Assess this cell for malaria.
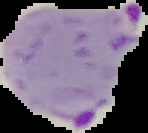

It is parasitized.

Image is 148×133 pixels. From a thin blood smear. Cell region segmented out of the field of view; the surrounding area is masked to black.